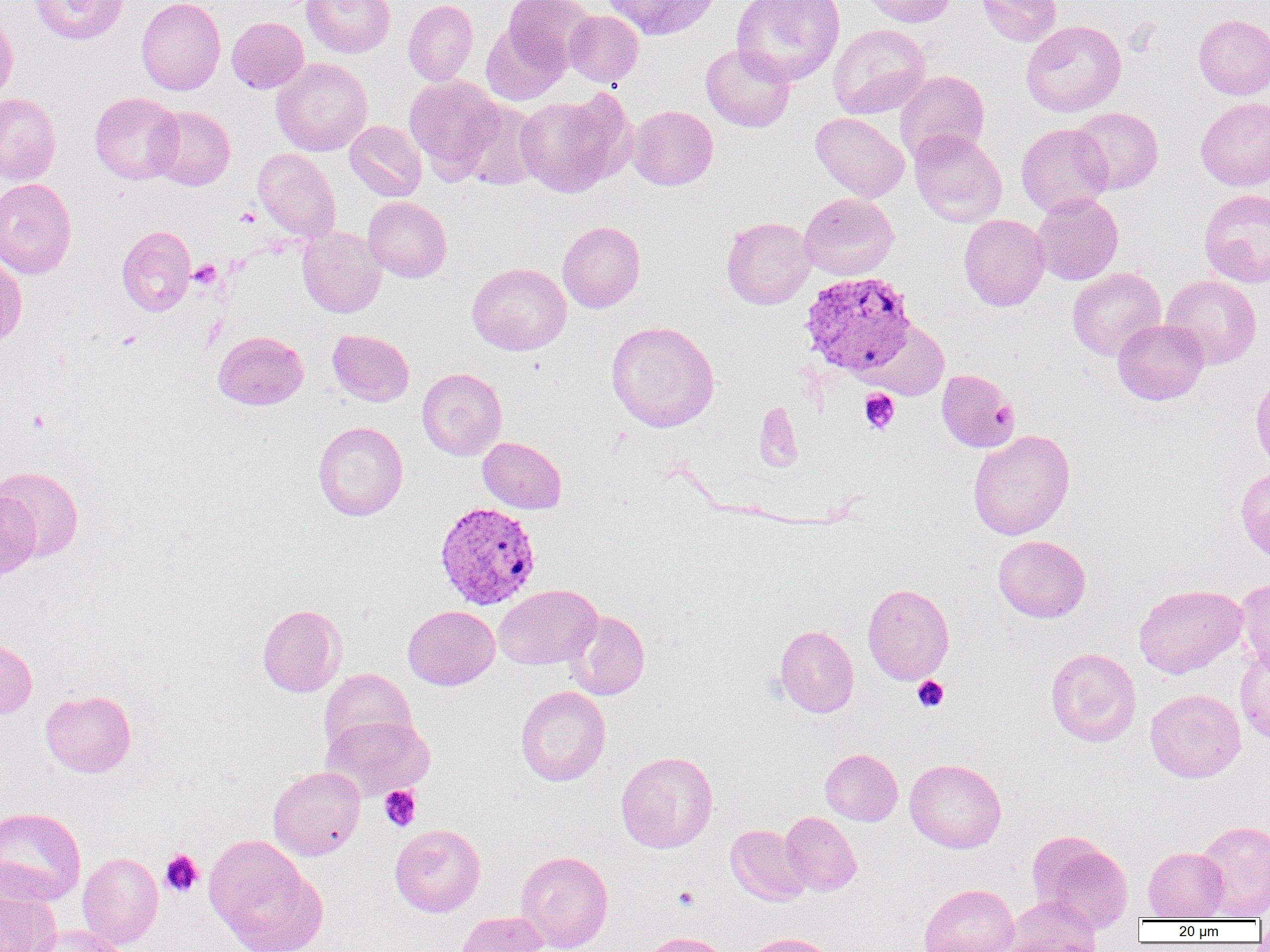

Approximate bounding boxes as [x1, y1, x2, y2] in pixels. Platelet locations: [236, 207, 259, 227], [189, 262, 221, 289], [116, 330, 142, 350], [859, 389, 900, 434], [27, 409, 50, 433], [912, 675, 950, 712], [379, 785, 422, 831], [160, 848, 204, 897], [674, 887, 700, 910]. Uninfected red blood cell locations: [28, 0, 128, 44], [136, 0, 225, 95], [303, 0, 395, 58], [403, 0, 478, 86], [503, 0, 595, 71], [602, 0, 718, 40], [732, 0, 845, 86], [862, 0, 957, 27], [976, 0, 1062, 46], [564, 10, 644, 87], [0, 11, 18, 106], [1193, 14, 1270, 99], [227, 16, 309, 93], [1021, 20, 1126, 117], [481, 21, 569, 105], [828, 24, 931, 119], [700, 43, 796, 132], [271, 57, 372, 156], [895, 70, 990, 164], [404, 74, 505, 177], [515, 91, 634, 198], [90, 92, 184, 184], [0, 93, 61, 185], [1195, 97, 1270, 190], [458, 100, 544, 190], [148, 105, 235, 190], [628, 105, 717, 190], [1070, 106, 1163, 194], [811, 113, 909, 202], [344, 120, 426, 201], [1016, 123, 1113, 217], [909, 129, 1007, 227], [253, 148, 341, 242], [0, 178, 77, 279], [1199, 189, 1270, 288], [1032, 192, 1123, 285], [799, 193, 899, 280], [363, 196, 452, 282], [959, 214, 1049, 311], [721, 216, 816, 309], [558, 221, 645, 312], [117, 225, 196, 316], [298, 226, 386, 318], [0, 257, 27, 348], [467, 262, 572, 355], [1067, 267, 1165, 360], [1161, 275, 1262, 369], [1113, 318, 1208, 405], [606, 321, 719, 432], [864, 321, 951, 399], [328, 329, 414, 406], [212, 330, 308, 410], [417, 368, 506, 460], [937, 369, 1019, 452], [1250, 371, 1270, 468], [754, 401, 802, 471], [313, 421, 408, 521], [967, 429, 1075, 540], [478, 436, 566, 513], [1, 466, 84, 562], [1236, 467, 1270, 563], [1, 492, 40, 579], [993, 535, 1091, 622], [1235, 578, 1270, 675], [862, 583, 954, 684], [494, 584, 602, 669], [1134, 584, 1246, 678], [257, 604, 347, 697], [403, 605, 500, 690], [563, 609, 650, 700], [774, 624, 859, 718], [0, 639, 37, 718], [1046, 647, 1141, 747], [1236, 648, 1270, 744], [320, 668, 416, 757], [515, 686, 611, 786], [1145, 689, 1246, 782], [40, 690, 137, 777], [321, 714, 434, 801], [820, 748, 903, 825], [616, 750, 718, 852], [905, 758, 1006, 853], [268, 766, 365, 860], [0, 807, 86, 905], [780, 812, 862, 896], [1195, 819, 1270, 920], [390, 824, 485, 917], [726, 824, 811, 906], [1028, 830, 1133, 933], [203, 834, 325, 952], [1143, 846, 1229, 920], [515, 850, 613, 951], [77, 852, 163, 949], [0, 879, 63, 952], [919, 883, 1020, 952], [1003, 896, 1103, 951], [453, 911, 549, 952], [27, 925, 129, 952], [637, 931, 734, 952], [742, 932, 839, 952]. Plasmodium vivax-infected red blood cell locations: [799, 271, 917, 377], [434, 502, 541, 610]. Slide-level diagnosis: Plasmodium vivax. Light microscopy. Thin blood smear. Captured at 1000x magnification. Single field of view. Image is 1270×952 pixels.